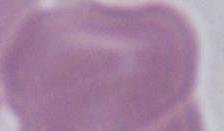
Summary:
  - Magnification: 1000x
  - Modality: micrograph
  - Identification: erythrocyte